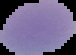

result = no Plasmodium parasites detected
image type = segmented cell region on a black background
image size = 76×55 pixels
preparation = thin blood film